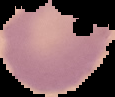

Summary:
  - Image size: 115×97 pixels
  - Result: no Plasmodium parasites seen
  - Image type: cell region segmented out of the field of view; surrounding area masked to black
  - Preparation: thin blood film